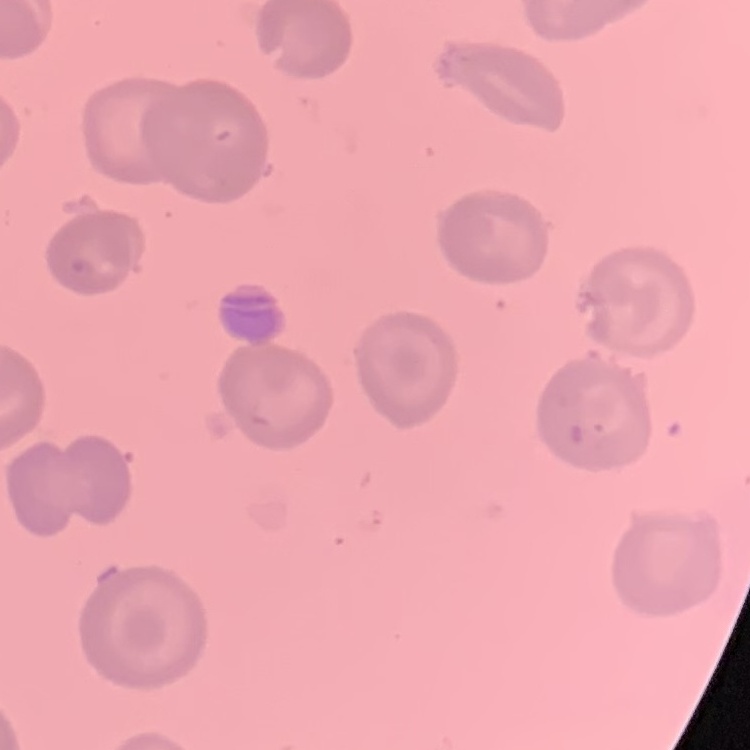

The red blood cells show no rouleaux formation. Field's or Giemsa stain. Square crop of a larger photomicrograph. Thin blood smear.